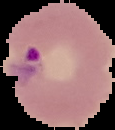 From a thin blood film. Cell region segmented out of the field of view; the surrounding area is masked to black. Result: Plasmodium parasites detected. Image is 115×130 pixels.